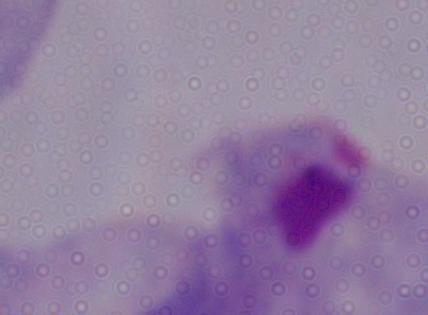

modality = photomicrograph
identification = trichomonad
magnification = 1000x